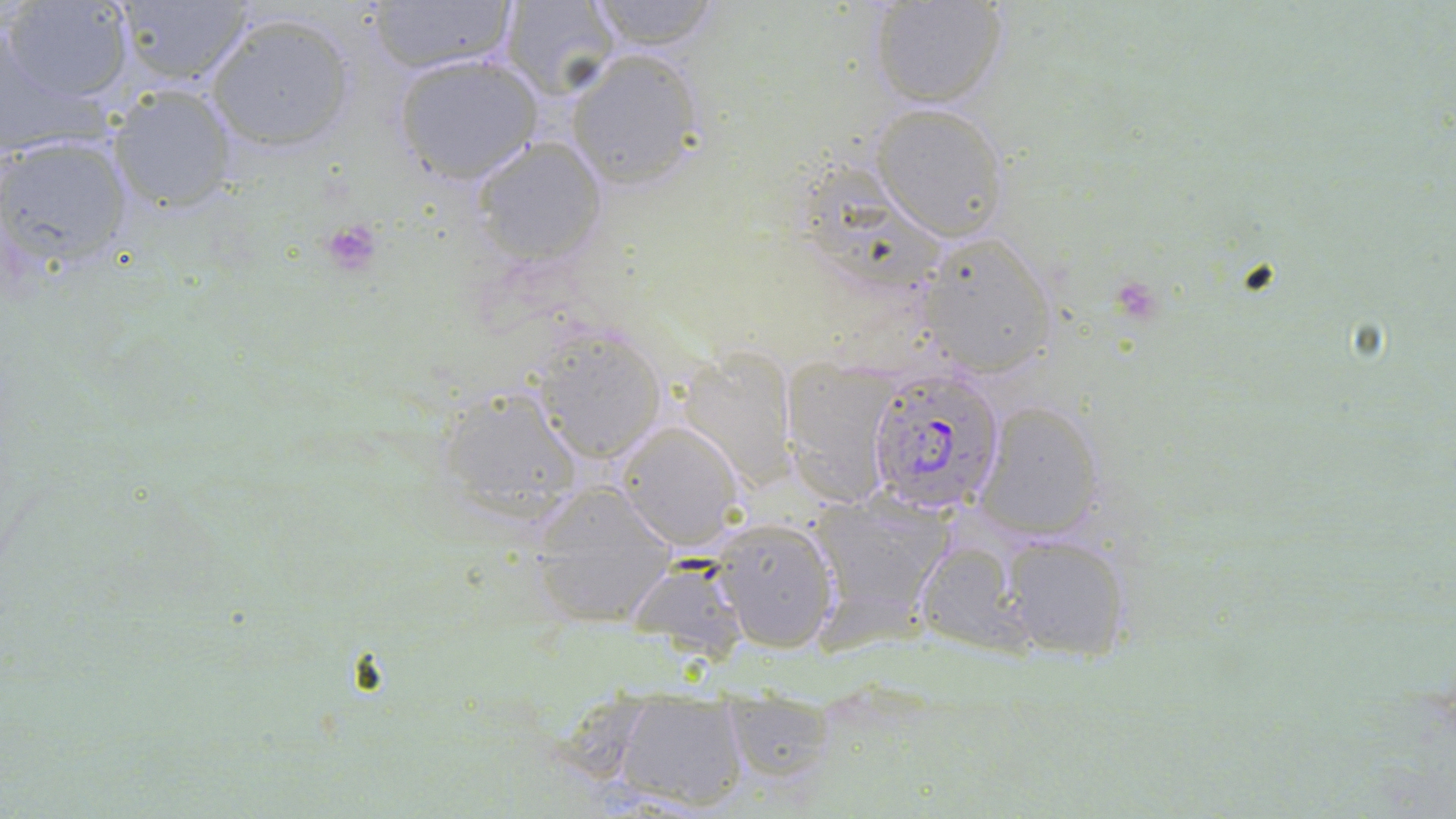

slide-level diagnosis = Plasmodium falciparum
stain = May-Grünwald-Giemsa
preparation = thin blood smear
platelet locations = approximate bounding boxes as (x1,y1)-(x2,y2) corner pairs in pixels: (318,219)-(383,275), (1121,283)-(1158,322)
magnification = 1000x
field of view = single
modality = light microscopy
uninfected red blood cell locations = approximate bounding boxes as (x1,y1)-(x2,y2) corner pairs in pixels: (2,0)-(136,106), (584,0)-(725,50), (868,0)-(1008,109), (112,1)-(256,89), (366,1)-(517,74), (497,1)-(623,98), (204,11)-(359,156), (0,22)-(59,157), (567,49)-(705,190), (392,53)-(543,185), (106,85)-(239,214), (870,104)-(1007,240), (1,133)-(135,273), (470,137)-(605,265), (796,160)-(950,290), (918,232)-(1057,375), (530,326)-(667,464), (676,349)-(798,491), (782,357)-(902,505), (434,385)-(586,526), (976,400)-(1106,542), (614,420)-(745,551), (524,481)-(681,628), (808,496)-(953,623), (710,517)-(840,654), (998,534)-(1134,664), (914,539)-(1028,656), (626,555)-(753,664), (614,692)-(751,813), (716,695)-(843,789)
Plasmodium falciparum-infected red blood cell locations = approximate bounding boxes as (x1,y1)-(x2,y2) corner pairs in pixels: (871,372)-(1006,515)
image size = 1456×819 pixels